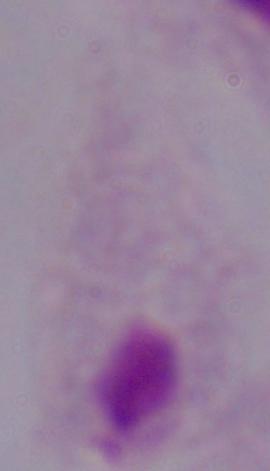

Summary:
  - Magnification: 1000x
  - Identification: trichomonad
  - Modality: photomicrograph